Report the malaria status of this cell.
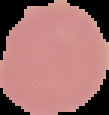

It is uninfected.

Summary:
  - Image size: 109×115 pixels
  - Preparation: thin blood smear
  - Image type: segmented cell region with the area outside set to black